Report the malaria status of this cell.
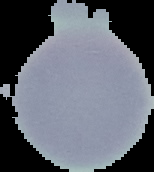

Uninfected.

preparation: thin blood smear
image_size: 154×172 pixels
image_type: segmented cell region on a black background